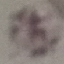

Result: no malaria parasites seen. Cell patch, automatically extracted from a larger field of view and resized to 64 × 64 pixels. Giemsa stain. Thin smear of blood. Acquired by smartphone through the microscope eyepiece.